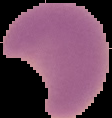
Image is 112×118 pixels. Segmented cell region on a black background. From a thin blood smear. Malaria status: parasitized.